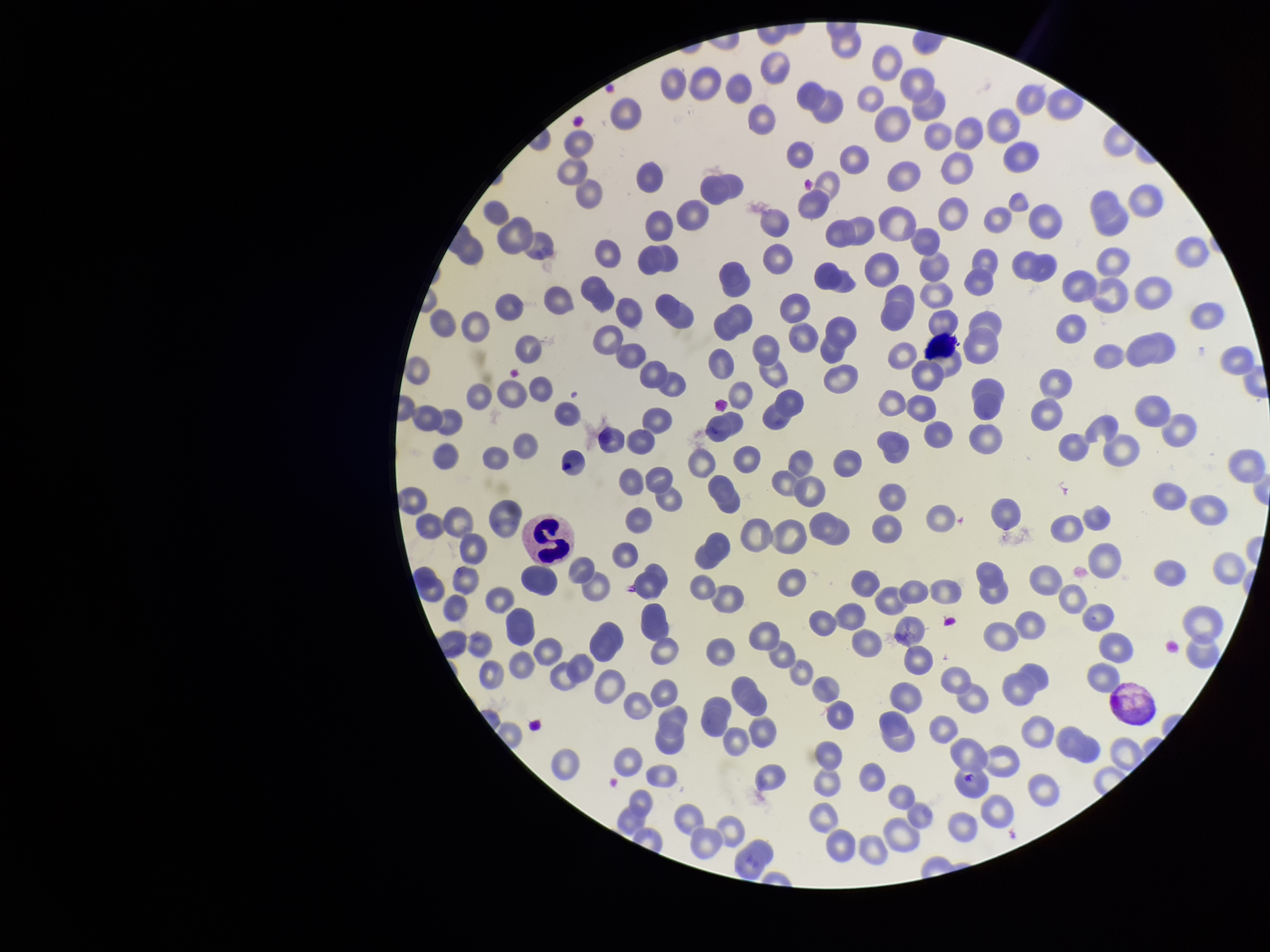
Summary:
  - Parasitized red blood cell count: 0
  - Stain: Giemsa
  - Red blood cell count: 222
  - Image size: 1270×952 pixels
  - Preparation: thin smear
  - Field of view: single
  - Patient malaria status: infected
  - Parasitized red blood cells: none seen
  - Species reported for this patient: Plasmodium vivax
  - Capture: smartphone photograph through the microscope eyepiece